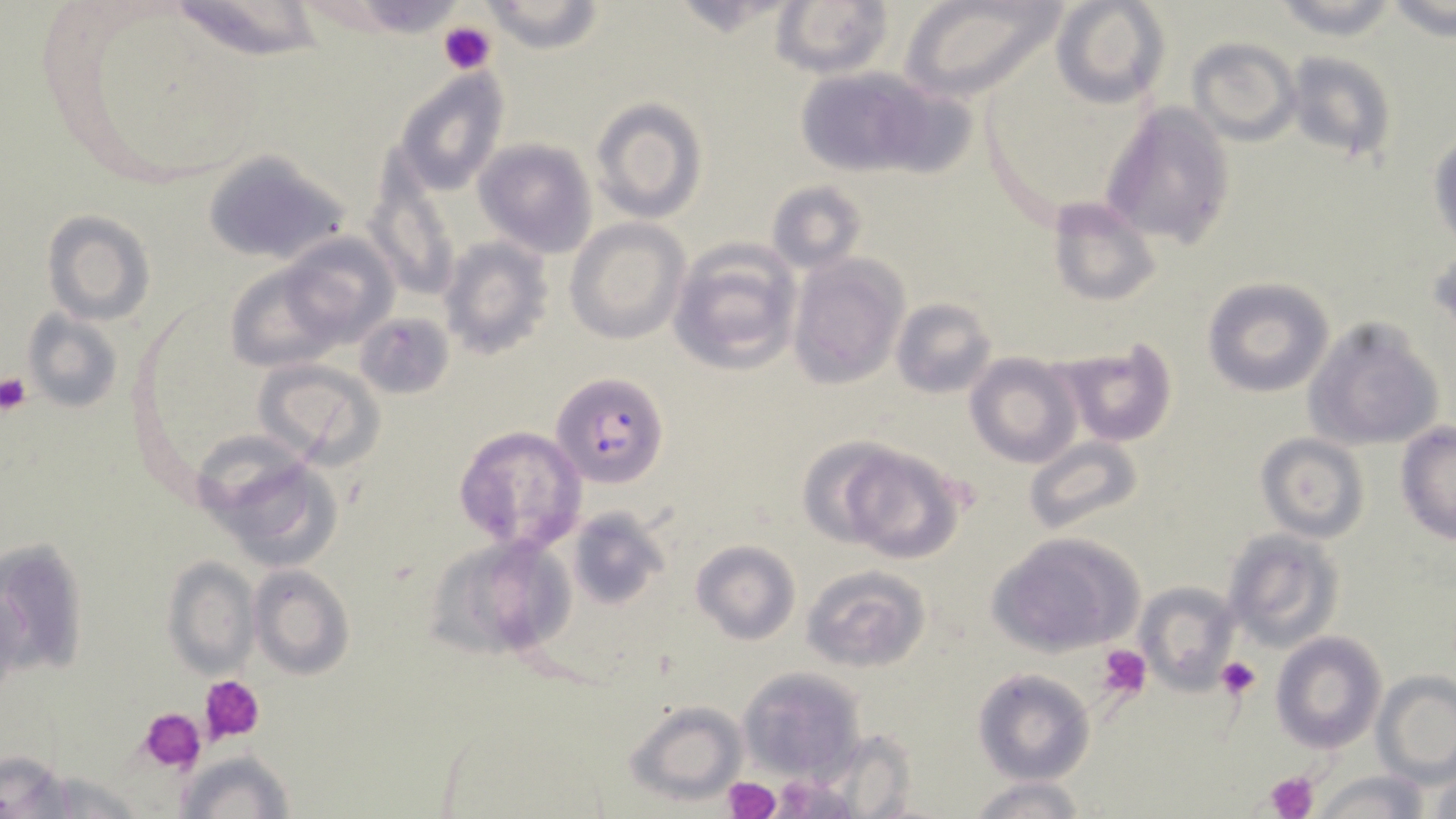

Approximate bounding boxes as (x1, y1, x2, y2) in pixels. Uninfected red blood cell locations: (162, 0, 329, 64), (899, 0, 1069, 105), (1050, 0, 1170, 109), (1269, 0, 1401, 39), (480, 1, 605, 54), (771, 1, 895, 80), (1385, 2, 1455, 46), (1188, 37, 1301, 147), (1283, 50, 1395, 165), (789, 64, 955, 181), (393, 68, 509, 196), (588, 98, 707, 224), (1101, 99, 1236, 251), (1429, 134, 1456, 247), (473, 139, 596, 255), (203, 149, 352, 265), (365, 176, 460, 301), (767, 180, 867, 274), (1047, 195, 1163, 307), (42, 210, 155, 325), (565, 219, 688, 343), (274, 232, 397, 348), (439, 236, 553, 359), (669, 238, 801, 374), (787, 256, 907, 389), (220, 258, 350, 374), (1200, 277, 1335, 397), (889, 295, 998, 399), (23, 309, 122, 414), (358, 312, 454, 401), (1302, 318, 1444, 450), (1056, 341, 1179, 447), (965, 353, 1083, 470), (254, 358, 386, 469), (1394, 422, 1456, 544), (453, 425, 586, 555), (1254, 432, 1370, 543), (797, 436, 910, 550), (1024, 438, 1144, 536), (837, 448, 963, 564), (211, 449, 344, 570), (567, 505, 667, 609), (1223, 529, 1344, 653), (988, 531, 1143, 657), (428, 532, 576, 661), (690, 540, 799, 644), (161, 556, 260, 677), (802, 563, 930, 672), (250, 564, 354, 679), (1134, 582, 1242, 693), (1272, 632, 1388, 753), (737, 666, 866, 782), (973, 669, 1094, 784), (1373, 672, 1456, 782), (622, 700, 745, 803), (819, 731, 917, 817), (174, 749, 296, 819), (1, 753, 74, 813), (1419, 758, 1456, 819), (28, 770, 149, 818), (1314, 772, 1430, 818), (965, 777, 1092, 819). Plasmodium falciparum-infected red blood cell locations: (552, 372, 669, 488). Platelet locations: (440, 17, 495, 74), (0, 373, 31, 415), (1098, 646, 1151, 697), (1216, 657, 1261, 700), (200, 675, 265, 744), (139, 710, 209, 774), (1266, 771, 1319, 819), (722, 776, 781, 819). Slide-level diagnosis: Plasmodium falciparum. One field of a larger specimen. Image is 1456×819 pixels. Thin blood film. Captured at 1000x magnification. May-Grünwald-Giemsa-stained preparation. Light microscopy.